Report the malaria status of this cell.
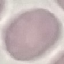
Uninfected.

Acquired by smartphone through the microscope eyepiece. Giemsa stain. Automatically extracted cell patch, resized to 64 × 64 pixels. Thin blood smear.